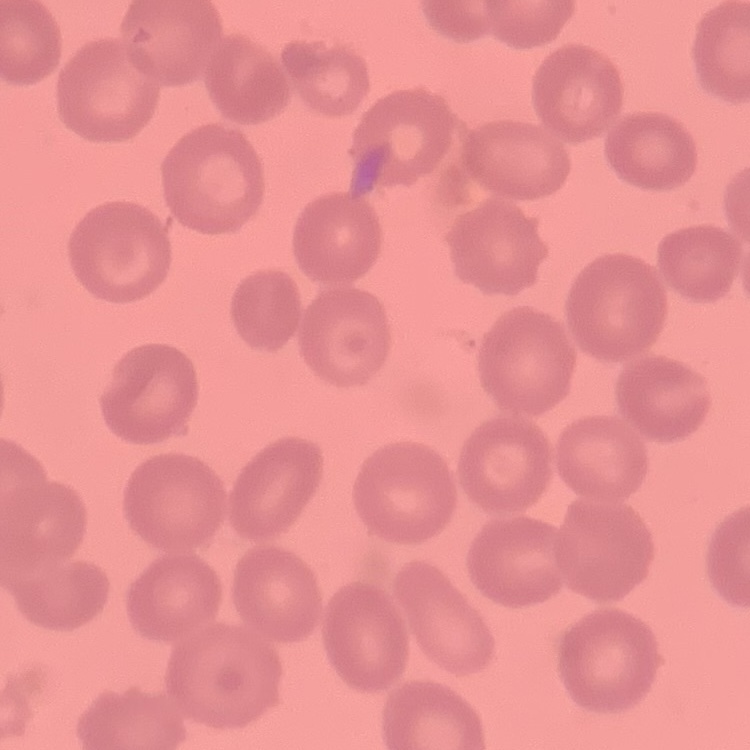
red blood cell morphology = no rouleaux formation
stain = Field's or Giemsa
image type = one tile cut from a larger photomicrograph
preparation = thin blood film